Locate every malaria parasite.
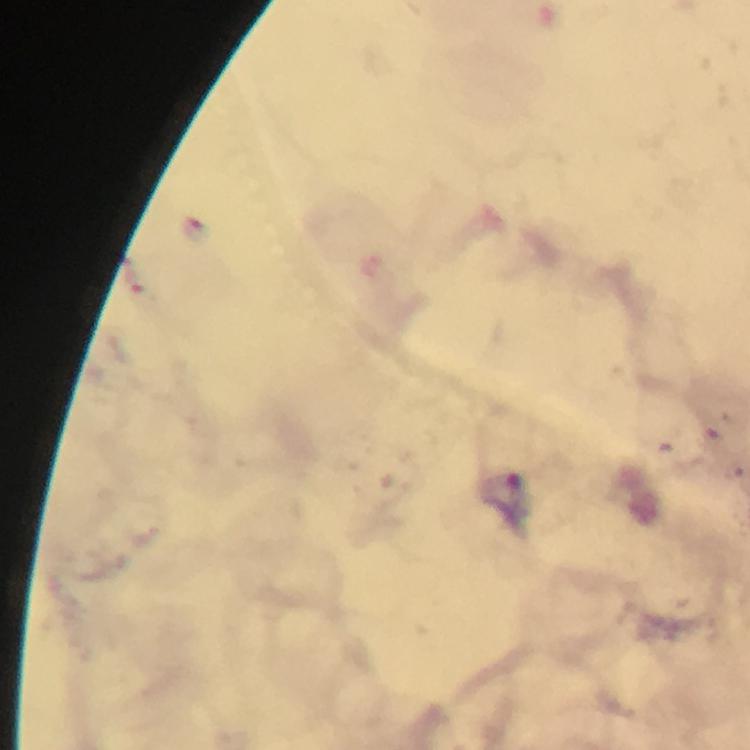
Approximate centers as {x, y} in pixels.
Malaria parasites: {194, 229}, {134, 282}.

image size = 750×750 pixels
cropped from = a single field of view
immersion oil = used
capture = smartphone camera through the microscope
magnification = 100x
preparation = thick blood film
context = from a malaria diagnostic workup
stain = Giemsa